Assess this cell for malaria.
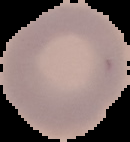
It is uninfected.

Image is 130×142 pixels. From a thin blood smear. Cell region segmented out of the field of view; the surrounding area is masked to black.